Assess this cell for malaria.
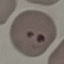

Parasitized.

Summary:
  - Capture: smartphone through the microscope eyepiece
  - Image type: automatically extracted cell patch, resized to 64 × 64 pixels
  - Stain: Giemsa
  - Preparation: thin smear